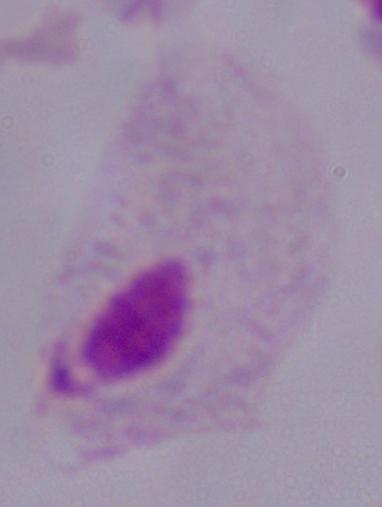
Captured at 1000x magnification. A trichomonad is seen. Photomicrograph.